Assess this cell for malaria.
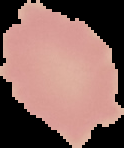

It is uninfected.

Summary:
  - Image type: segmented cell region with the area outside set to black
  - Image size: 124×148 pixels
  - Preparation: thin blood film